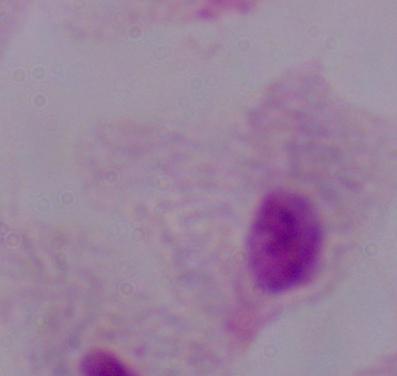
identification: trichomonad
magnification: 1000x
modality: micrograph